Name the parasite shown.
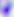

Toxoplasma gondii.

Summary:
  - Modality: micrograph
  - Magnification: 400x